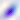
Captured at 400x magnification. Photomicrograph. Toxoplasma gondii is seen.